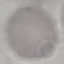
Summary:
  - Malaria status: uninfected
  - Preparation: thin smear
  - Image type: cell patch, automatically extracted from a larger field of view and resized to 64 × 64 pixels
  - Stain: Giemsa
  - Capture: smartphone through the microscope eyepiece